Classify this cell by malaria status.
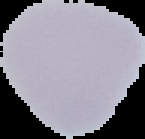

It is uninfected.

Image is 145×139 pixels. The area outside the segmented cell region is set to black. From a thin blood film.